Assess this cell for malaria.
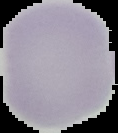
It is uninfected.

The area outside the segmented cell region is set to black. Image is 118×133 pixels. From a thin blood smear.